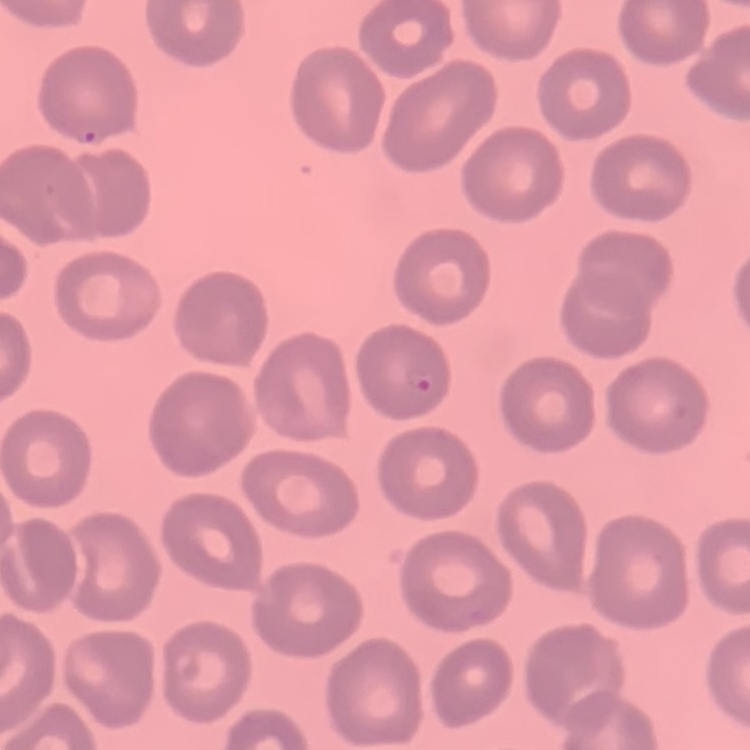
Summary:
  - Erythrocyte morphology: no rouleaux formation
  - Image type: square crop of a larger photomicrograph
  - Stain: Field's or Giemsa
  - Preparation: thin peripheral smear